Assess for malaria.
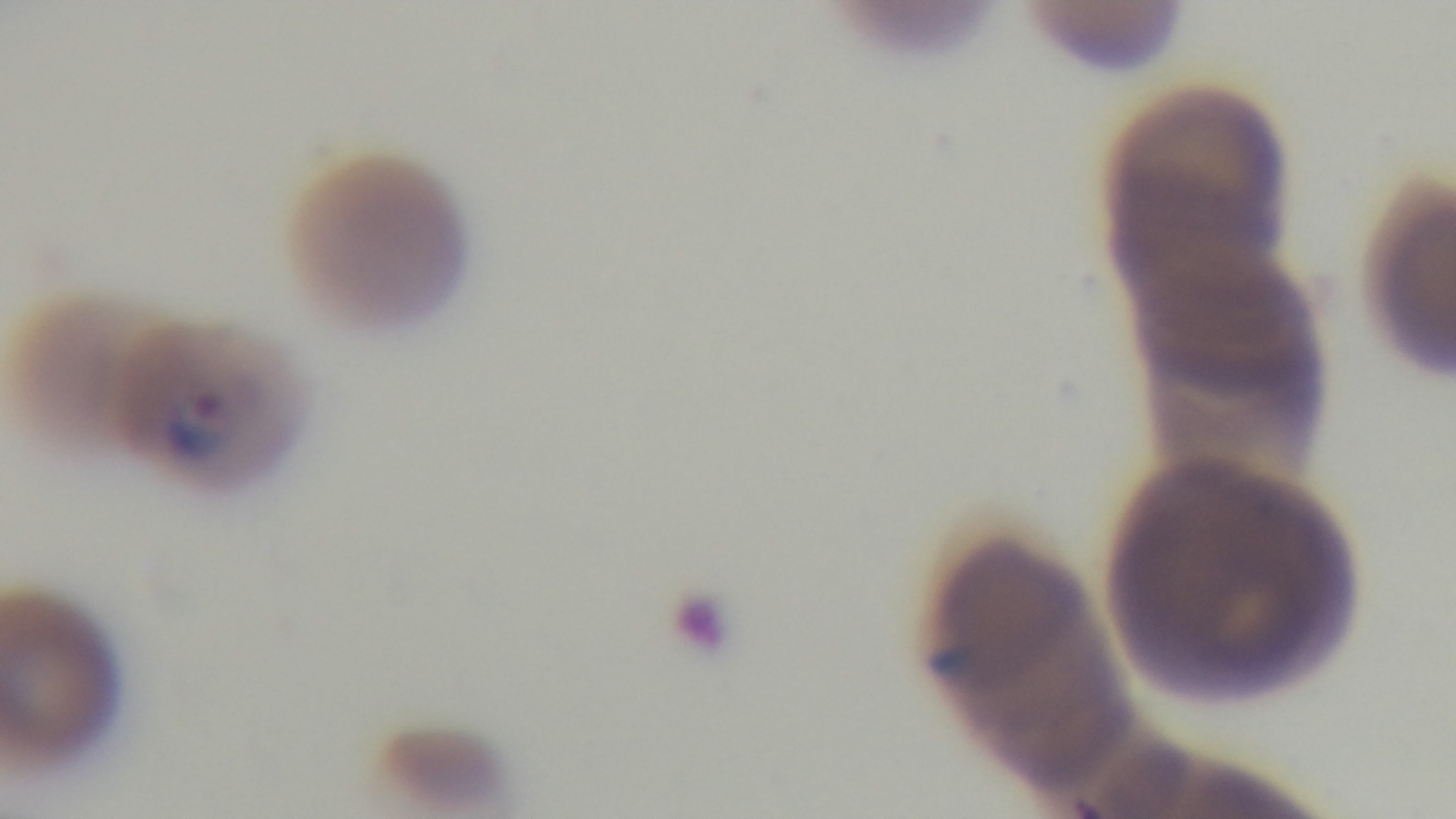
It is infected.

Single field of view. 100x oil-immersion objective. Preparation: thin. Giemsa-stained. Light microscopy. Mounted 4K digital camera.